Classify this cell by malaria status.
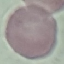

Uninfected.

{
  "stain": "Giemsa",
  "image_type": "cell patch, automatically extracted from a larger field of view and resized to 64 × 64 pixels",
  "capture": "smartphone camera at the microscope eyepiece",
  "preparation": "thin blood smear"
}